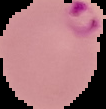
The area outside the segmented cell region is set to black. From a thin blood film. Result: Plasmodium parasites detected. Image is 106×109 pixels.